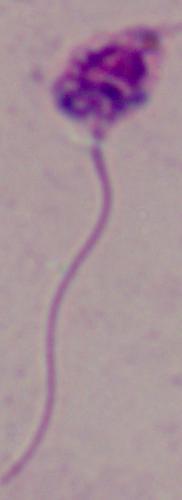
Summary:
  - Magnification: 1000x
  - Modality: micrograph
  - Identification: Leishmania